Assess the morphology of the red blood cells.
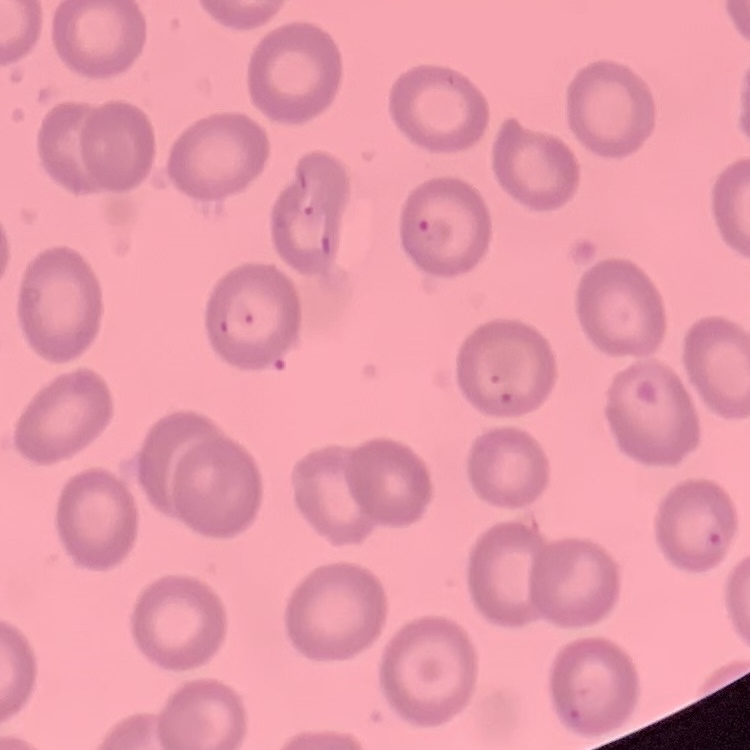

No rouleaux formation.

Summary:
  - Stain: Field's or Giemsa
  - Preparation: thin blood smear
  - Image type: one tile cut from a larger photomicrograph